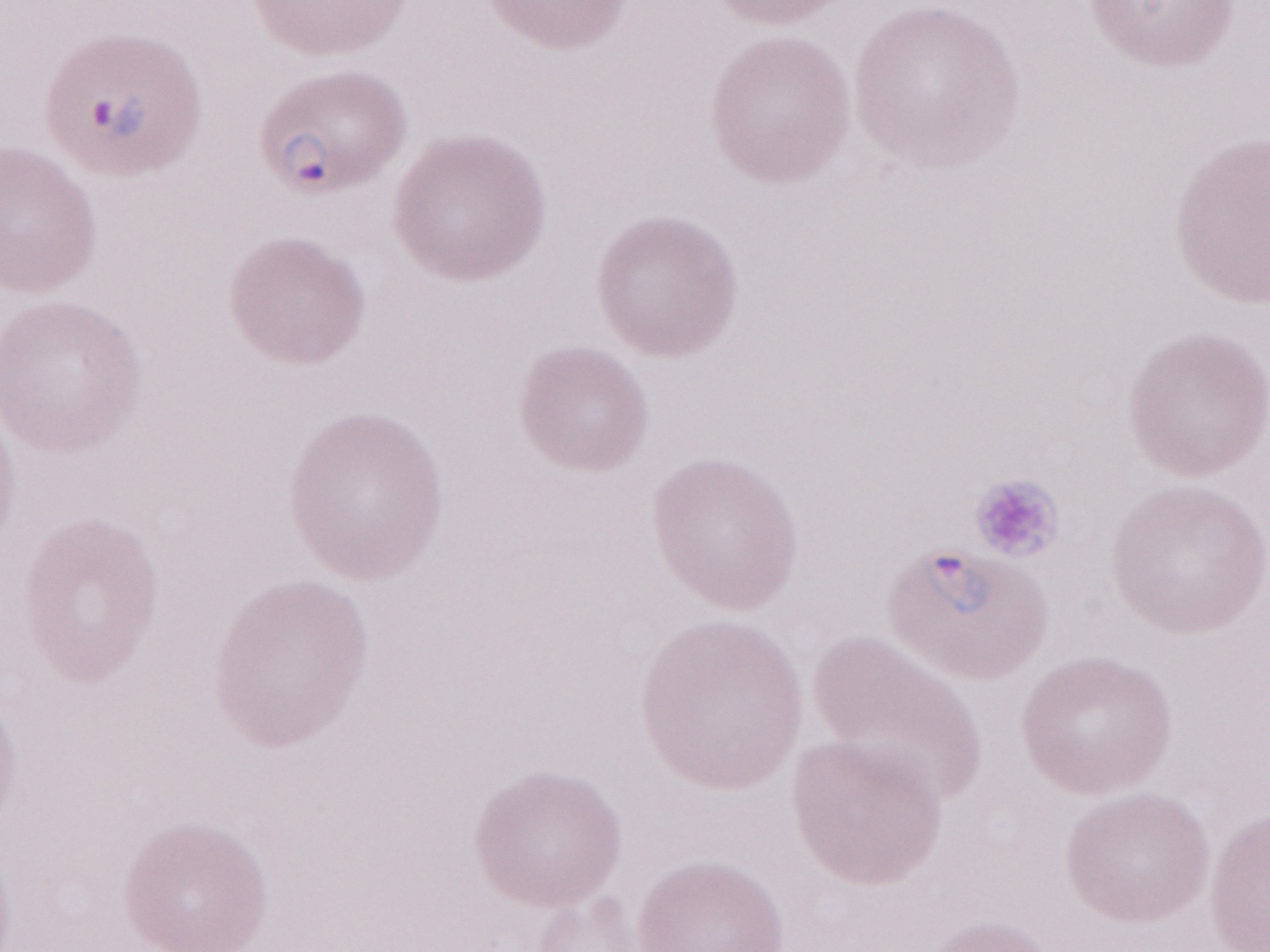 Image is 1270×952 pixels. Single field of view. Thin blood film. Olympus BX43 microscope, Olympus DP73 camera. Patient-level malaria diagnosis: positive. Magnification: 1,000x. May-Grünwald-Giemsa-stained preparation.